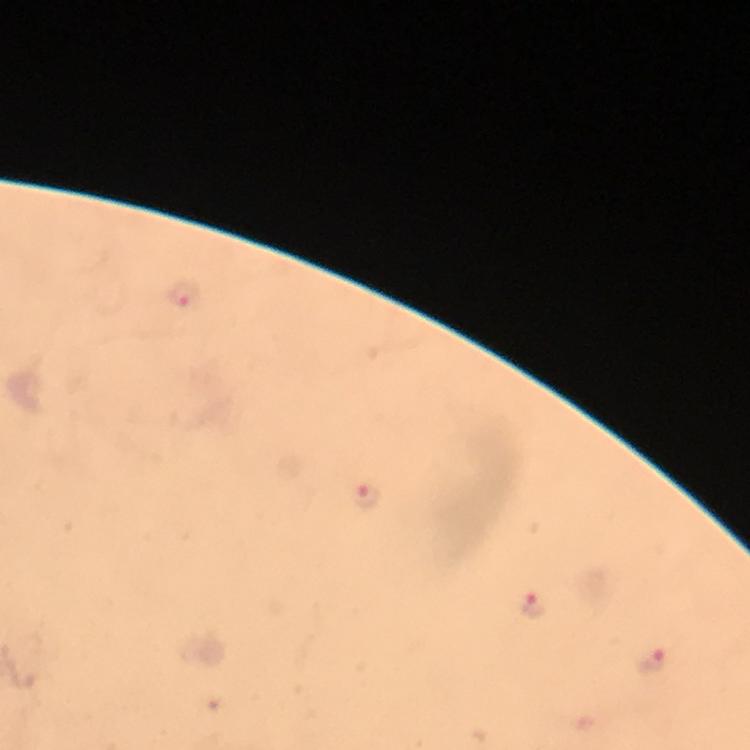

Approximate centers as {x, y} in pixels.
Summary:
  - Plasmodium parasite locations: {183, 294}, {366, 496}, {534, 605}, {652, 660}
  - Magnification: 100x
  - Immersion oil: applied
  - Preparation: thick blood film
  - Stain: Giemsa
  - Context: from a diagnostic examination for malaria
  - Image size: 750×750 pixels
  - Capture: smartphone photograph through a microscope
  - Cropped from: one field of view